Comment on the morphology of the erythrocytes.
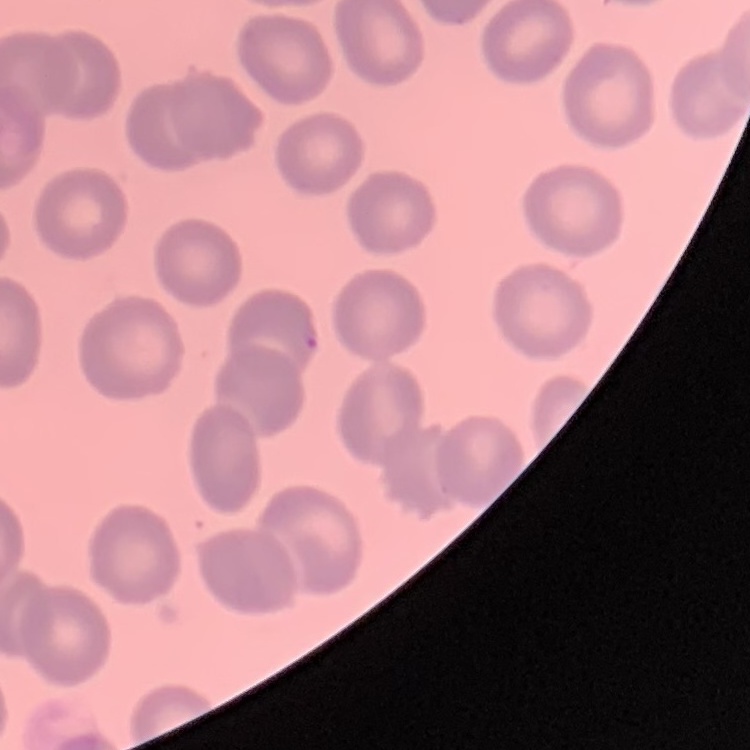

No rouleaux formation.

image_type: one tile cut from a larger photomicrograph
preparation: thin blood film
stain: Field's or Giemsa